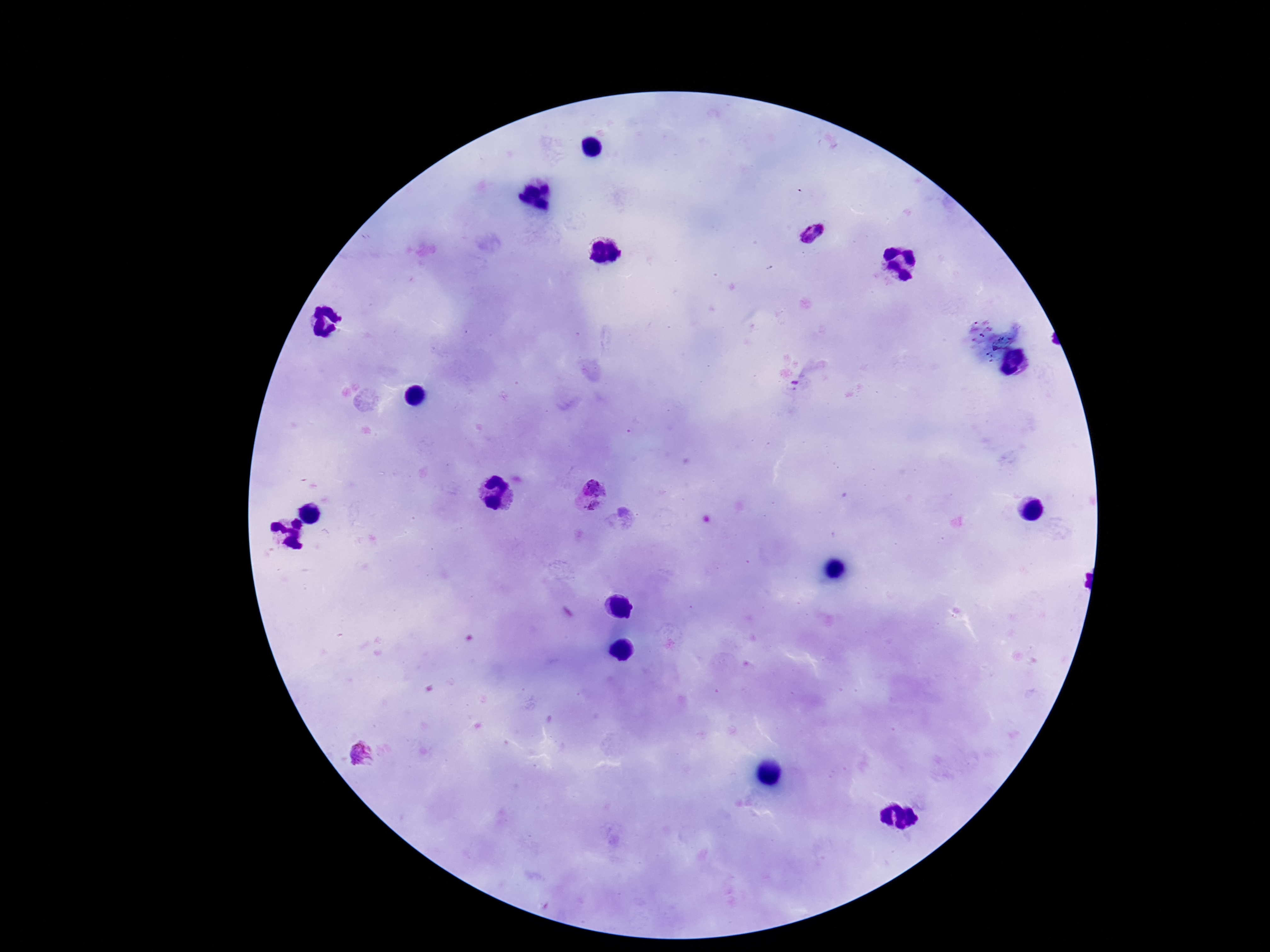
Plasmodium parasite locations = approximate centers as (x, y) in pixels: (814, 234), (591, 495)
capture = smartphone camera through the microscope eyepiece
patient malaria status = infected
stain = Giemsa
field of view = one from this slide
image size = 1270×952 pixels
magnification = 100x
preparation = thick blood film